Assess this cell for malaria.
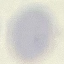

Uninfected.

Photographed with a smartphone camera at the microscope eyepiece. Automatically extracted cell patch, resized to 64 × 64 pixels. Thin blood smear. Giemsa stain.